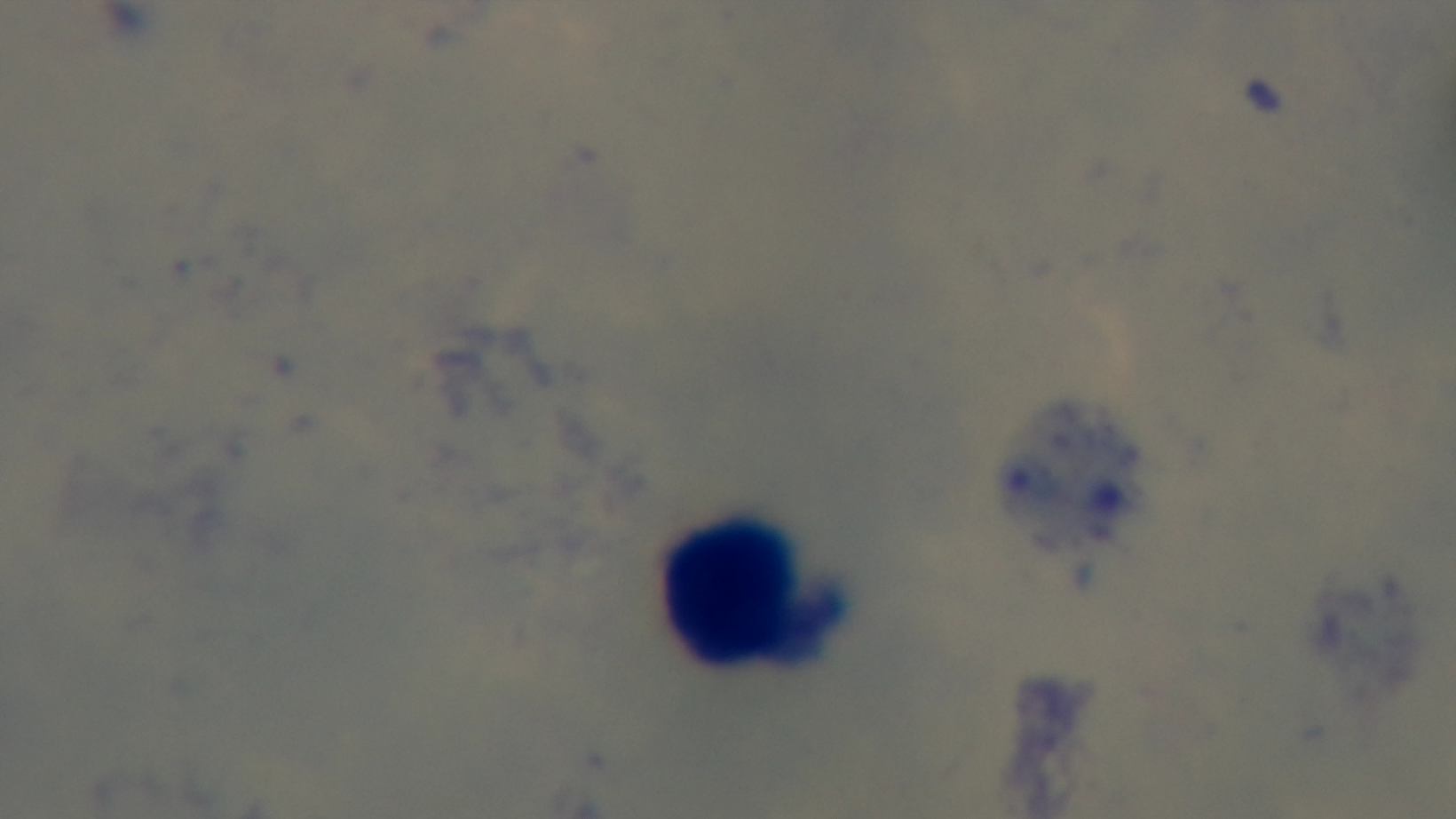

Preparation: thick blood film. Giemsa stain. Oil-immersion objective, 100x. Photomicrograph. Captured with a mounted 4K digital camera. Malaria status: uninfected. One field from the slide.